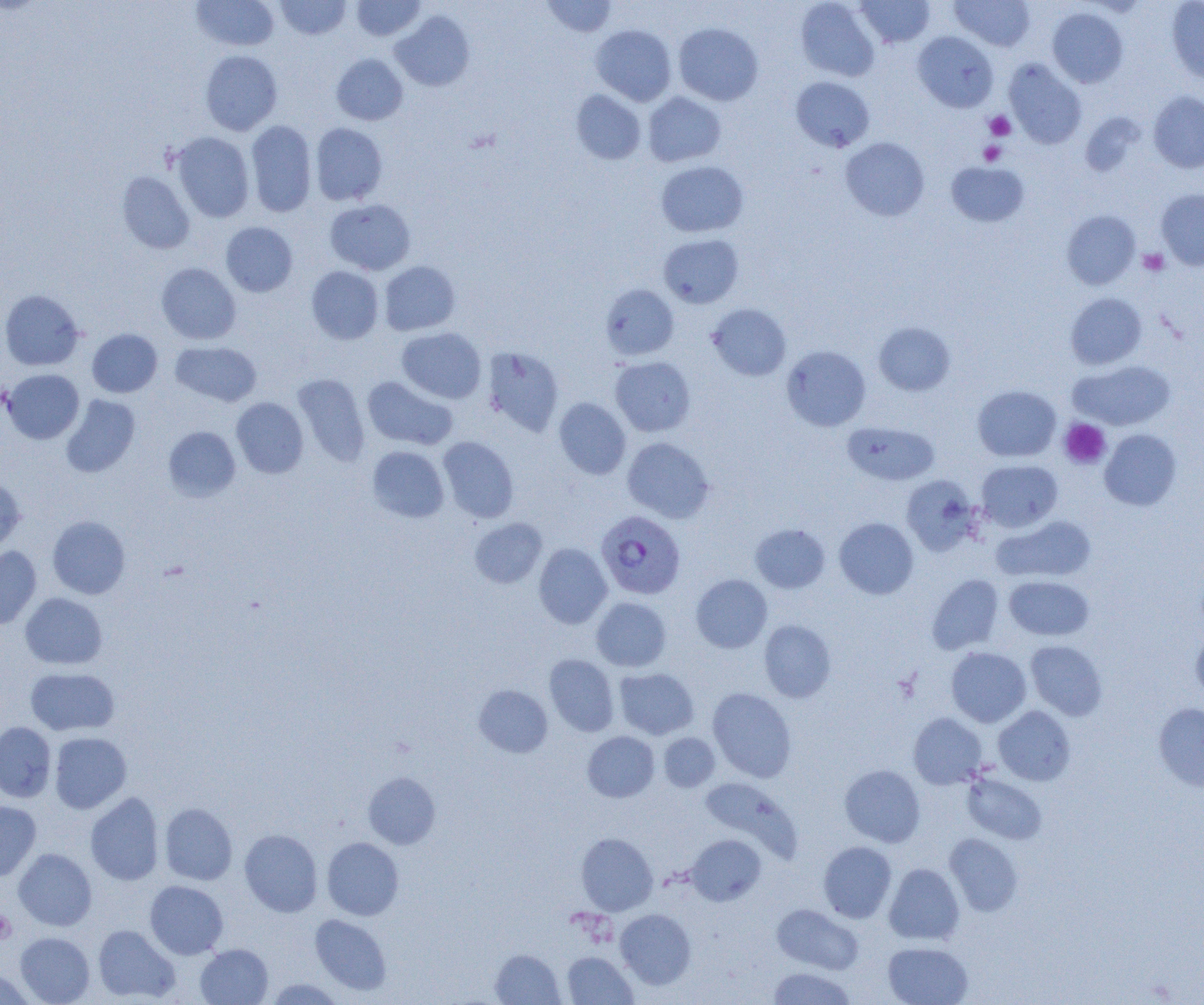
slide-level diagnosis = Plasmodium falciparum
image size = 1204×1005 pixels
magnification = 1000x
uninfected red blood cell locations = approximate bounding boxes as (x1, y1, x2, y2) in pixels: (192, 0, 279, 51), (275, 0, 351, 39), (352, 0, 426, 41), (541, 0, 617, 38), (795, 0, 880, 82), (857, 0, 934, 47), (950, 0, 1035, 51), (1167, 1, 1204, 83), (1047, 7, 1128, 88), (390, 10, 474, 91), (673, 23, 763, 106), (591, 24, 676, 106), (913, 31, 997, 112), (200, 50, 283, 135), (331, 54, 408, 125), (1004, 58, 1086, 148), (791, 76, 874, 152), (571, 90, 646, 164), (1148, 91, 1204, 173), (642, 92, 725, 167), (246, 120, 317, 217), (310, 123, 388, 205), (171, 132, 255, 222), (841, 137, 929, 220), (656, 161, 748, 237), (946, 161, 1029, 227), (116, 171, 195, 254), (1156, 188, 1204, 270), (325, 199, 416, 274), (1062, 210, 1140, 289), (221, 222, 297, 297), (658, 234, 744, 308), (379, 261, 460, 335), (156, 263, 241, 344), (306, 266, 383, 344), (600, 284, 679, 360), (0, 290, 84, 371), (1066, 293, 1147, 369), (707, 303, 791, 381), (873, 321, 956, 396), (397, 327, 486, 403), (87, 329, 162, 397), (170, 341, 262, 406), (781, 345, 871, 431), (481, 346, 564, 436), (610, 356, 695, 436), (1069, 360, 1175, 431), (2, 369, 84, 444), (292, 374, 370, 466), (362, 376, 458, 450), (973, 385, 1061, 461), (61, 394, 141, 478), (231, 397, 308, 478), (553, 397, 631, 479), (842, 421, 939, 485), (163, 426, 241, 502), (1100, 429, 1181, 510), (438, 436, 519, 522), (622, 437, 714, 522), (367, 446, 450, 522), (976, 459, 1063, 532), (902, 475, 981, 556), (0, 477, 26, 553), (993, 515, 1096, 583), (47, 516, 130, 599), (834, 517, 919, 599), (470, 518, 547, 588), (750, 523, 830, 593), (533, 543, 612, 628), (0, 546, 41, 629), (691, 574, 772, 653), (927, 574, 1004, 654), (1004, 575, 1094, 641), (20, 592, 108, 670), (591, 597, 672, 671), (759, 620, 836, 702), (1191, 631, 1204, 704), (1026, 640, 1107, 720), (945, 647, 1031, 727), (544, 654, 619, 737), (25, 667, 120, 735), (614, 668, 699, 739), (474, 685, 552, 757), (708, 687, 796, 782), (1153, 703, 1204, 792), (994, 706, 1075, 785), (908, 713, 987, 789), (0, 722, 56, 802), (582, 731, 659, 802), (49, 732, 131, 813), (659, 733, 720, 792), (839, 764, 925, 847), (363, 772, 441, 849), (962, 772, 1047, 844), (699, 777, 801, 861), (85, 792, 164, 886), (0, 800, 41, 881), (159, 803, 237, 885), (240, 829, 322, 917), (576, 833, 658, 915), (944, 833, 1023, 916), (685, 834, 766, 906), (322, 837, 404, 920), (818, 841, 896, 923), (13, 848, 97, 930), (884, 863, 964, 944), (145, 880, 228, 959), (772, 904, 864, 974), (615, 909, 696, 989), (310, 914, 392, 995), (93, 925, 180, 1003), (15, 932, 95, 1004), (883, 941, 973, 1005), (195, 944, 273, 1004), (490, 949, 564, 1005), (562, 951, 637, 1004), (767, 967, 857, 1004), (0, 968, 34, 1004), (265, 978, 345, 1004)
preparation = thin blood film
field of view = single
platelet locations = approximate bounding boxes as (x1, y1, x2, y2) in pixels: (984, 111, 1015, 140), (979, 141, 1005, 165), (1138, 248, 1168, 275), (1059, 418, 1110, 469), (0, 910, 16, 943)
modality = light microscopy
Plasmodium falciparum-infected red blood cell locations = approximate bounding boxes as (x1, y1, x2, y2) in pixels: (596, 511, 685, 599)